Outline each blood parasite and name the species.
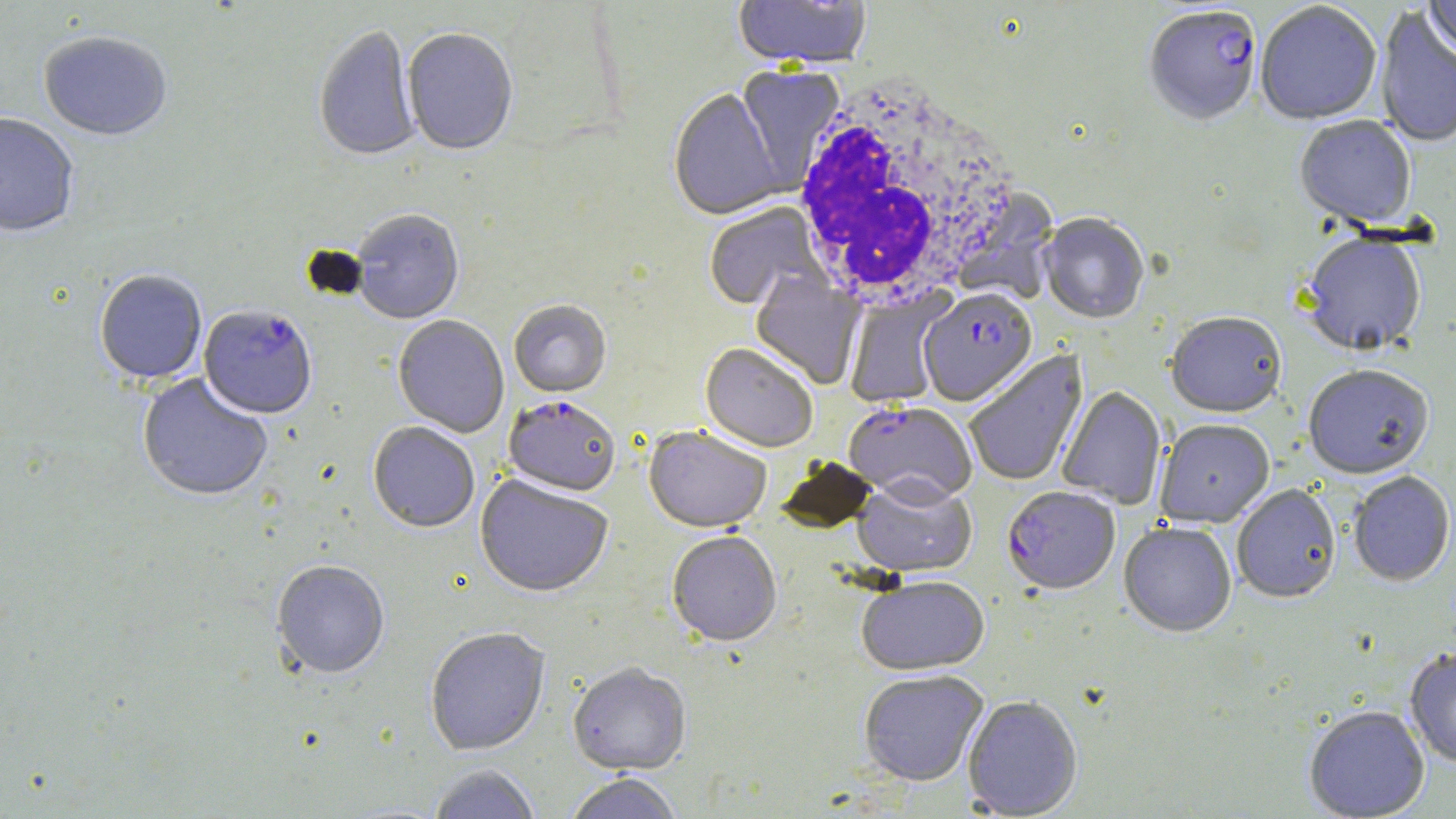
Approximate bounding boxes as named x1/y1/x2/y2 corners in pixels.
Plasmodium falciparum-infected red blood cells: (x1=1143, y1=8, x2=1262, y2=129), (x1=920, y1=289, x2=1038, y2=408), (x1=199, y1=308, x2=317, y2=421), (x1=502, y1=397, x2=620, y2=499), (x1=844, y1=403, x2=977, y2=507), (x1=1002, y1=487, x2=1120, y2=597).
No Plasmodium ovale, Plasmodium malariae, Plasmodium vivax, Babesia divergens, or Trypanosoma brucei observed.

slide-level diagnosis = Plasmodium falciparum
stain = May-Grünwald-Giemsa
image size = 1456×819 pixels
modality = light microscopy
field of view = single
magnification = 1000x
uninfected red blood cell locations = approximate bounding boxes as named x1/y1/x2/y2 corners in pixels: (x1=1423, y1=0, x2=1456, y2=61), (x1=733, y1=1, x2=872, y2=72), (x1=1256, y1=3, x2=1382, y2=127), (x1=1374, y1=7, x2=1456, y2=150), (x1=313, y1=26, x2=421, y2=165), (x1=402, y1=30, x2=519, y2=159), (x1=39, y1=34, x2=172, y2=144), (x1=735, y1=65, x2=845, y2=192), (x1=668, y1=89, x2=786, y2=223), (x1=0, y1=116, x2=78, y2=241), (x1=1294, y1=117, x2=1417, y2=231), (x1=704, y1=203, x2=828, y2=313), (x1=351, y1=211, x2=465, y2=326), (x1=1039, y1=215, x2=1149, y2=326), (x1=1300, y1=236, x2=1427, y2=359), (x1=95, y1=272, x2=207, y2=386), (x1=750, y1=272, x2=866, y2=391), (x1=844, y1=289, x2=952, y2=408), (x1=509, y1=302, x2=611, y2=399), (x1=1165, y1=314, x2=1286, y2=420), (x1=392, y1=316, x2=509, y2=439), (x1=699, y1=345, x2=818, y2=454), (x1=964, y1=350, x2=1089, y2=488), (x1=1302, y1=366, x2=1434, y2=482), (x1=136, y1=375, x2=271, y2=504), (x1=1056, y1=386, x2=1167, y2=510), (x1=1155, y1=420, x2=1274, y2=529), (x1=368, y1=424, x2=479, y2=534), (x1=643, y1=428, x2=771, y2=536), (x1=775, y1=456, x2=878, y2=536), (x1=1348, y1=472, x2=1455, y2=588), (x1=474, y1=476, x2=614, y2=601), (x1=851, y1=478, x2=977, y2=580), (x1=1232, y1=486, x2=1340, y2=605), (x1=1118, y1=523, x2=1236, y2=638), (x1=666, y1=533, x2=782, y2=649), (x1=271, y1=562, x2=390, y2=681), (x1=857, y1=578, x2=990, y2=677), (x1=425, y1=629, x2=551, y2=757), (x1=1404, y1=648, x2=1456, y2=769), (x1=567, y1=665, x2=691, y2=778), (x1=858, y1=672, x2=988, y2=787), (x1=962, y1=697, x2=1083, y2=817), (x1=1304, y1=707, x2=1430, y2=819), (x1=428, y1=766, x2=541, y2=819), (x1=564, y1=775, x2=683, y2=819)
white blood cell locations = approximate bounding boxes as named x1/y1/x2/y2 corners in pixels: (x1=790, y1=78, x2=1026, y2=309), (x1=708, y1=201, x2=827, y2=314)
preparation = thin blood film